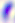
identification = Toxoplasma gondii
modality = photomicrograph
magnification = 400x